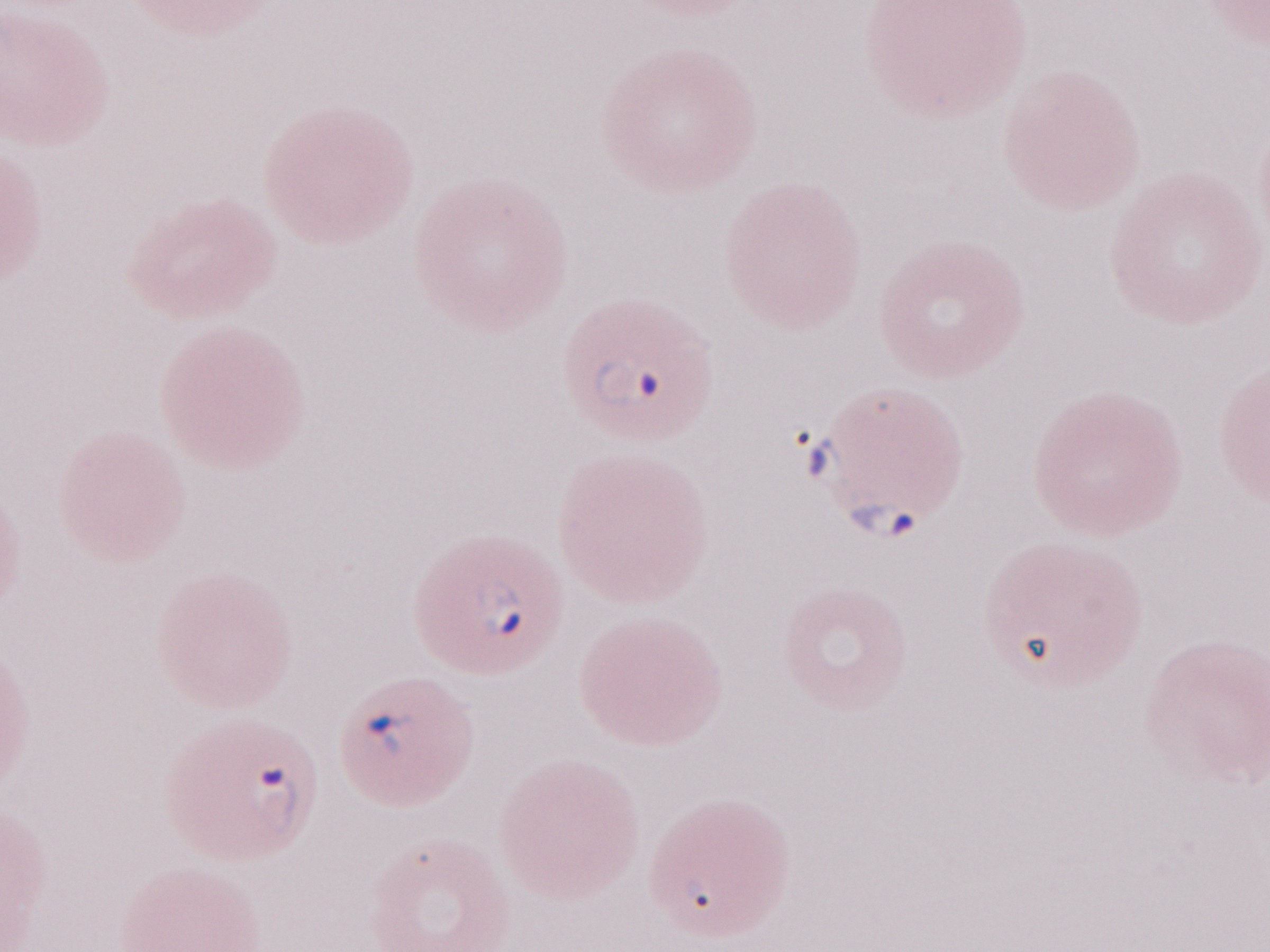
May-Grünwald-Giemsa (MGG) stain. Single field of view. 1,000x magnification. Patient diagnosis: malaria infection. Image is 1270×952 pixels. Olympus BX43 microscope and DP73 digital camera. Thin peripheral-blood smear.